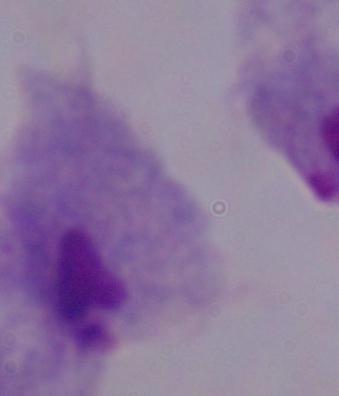
{
  "modality": "micrograph",
  "identification": "trichomonad",
  "magnification": "1000x"
}